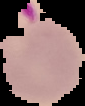
Summary:
  - Image type: segmented cell region on a black background
  - Image size: 85×106 pixels
  - Preparation: thin blood smear
  - Malaria status: parasitized